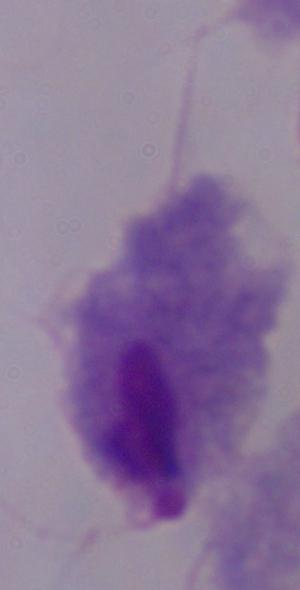

1000x magnification. Micrograph. A trichomonad is shown.